Evaluate for malaria.
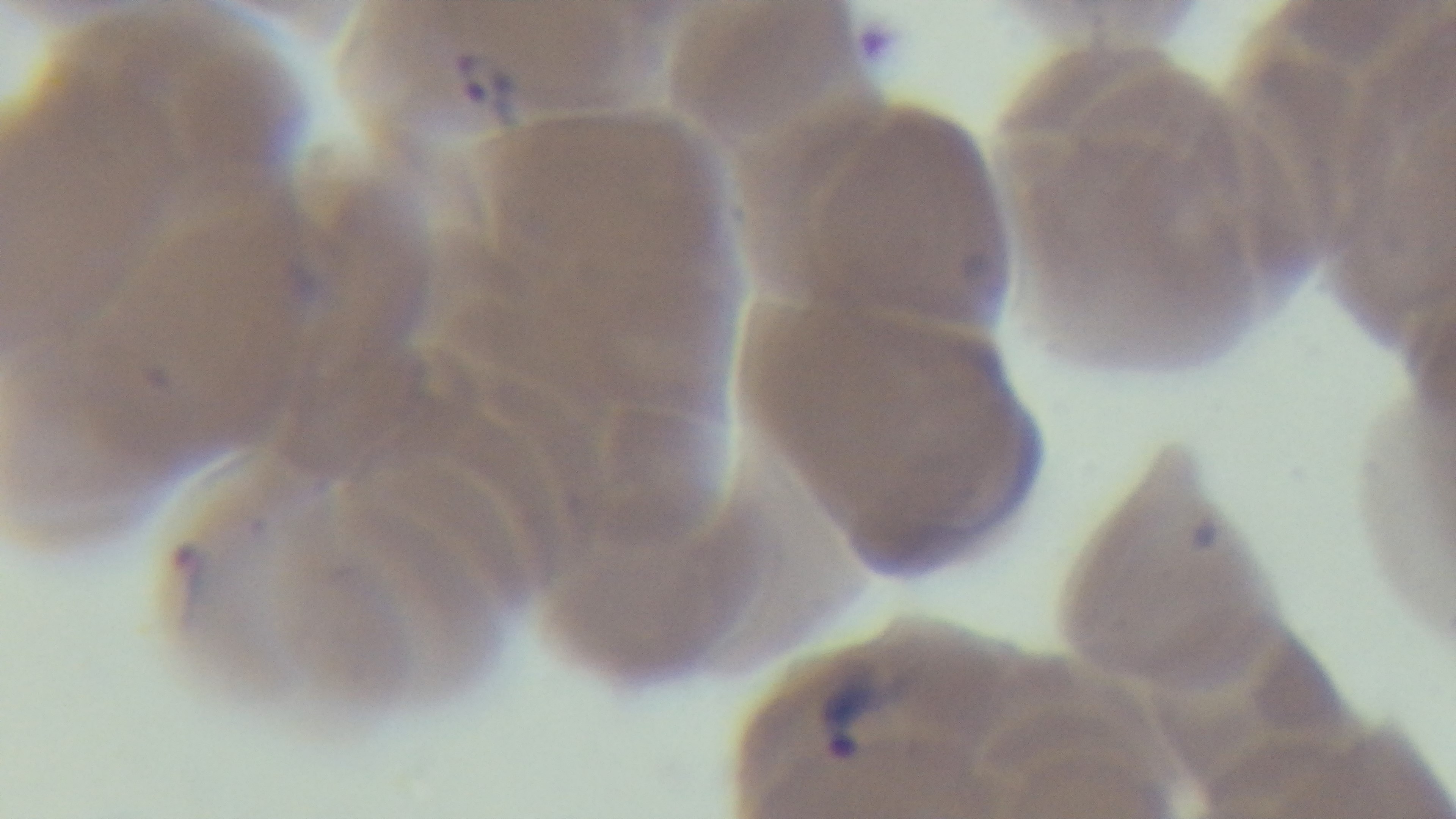
It is infected.

Summary:
  - Modality: light microscopy
  - Stain: Giemsa
  - Capture: mounted 4K digital camera
  - Objective: 100x oil immersion
  - Field of view: one from the slide
  - Preparation: thin blood film